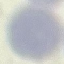
Summary:
  - Malaria status: uninfected
  - Capture: smartphone camera at the microscope eyepiece
  - Image type: automatically extracted cell patch, resized to 64 × 64 pixels
  - Stain: Giemsa
  - Preparation: thin smear